Identify the parasite.
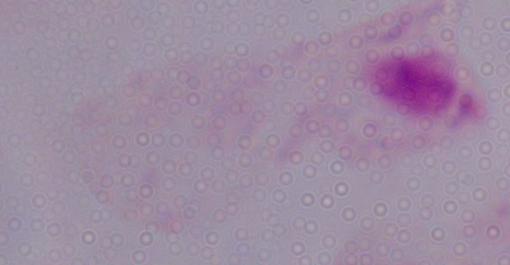

A trichomonad.

modality = micrograph
magnification = 1000x